Evaluate for malaria.
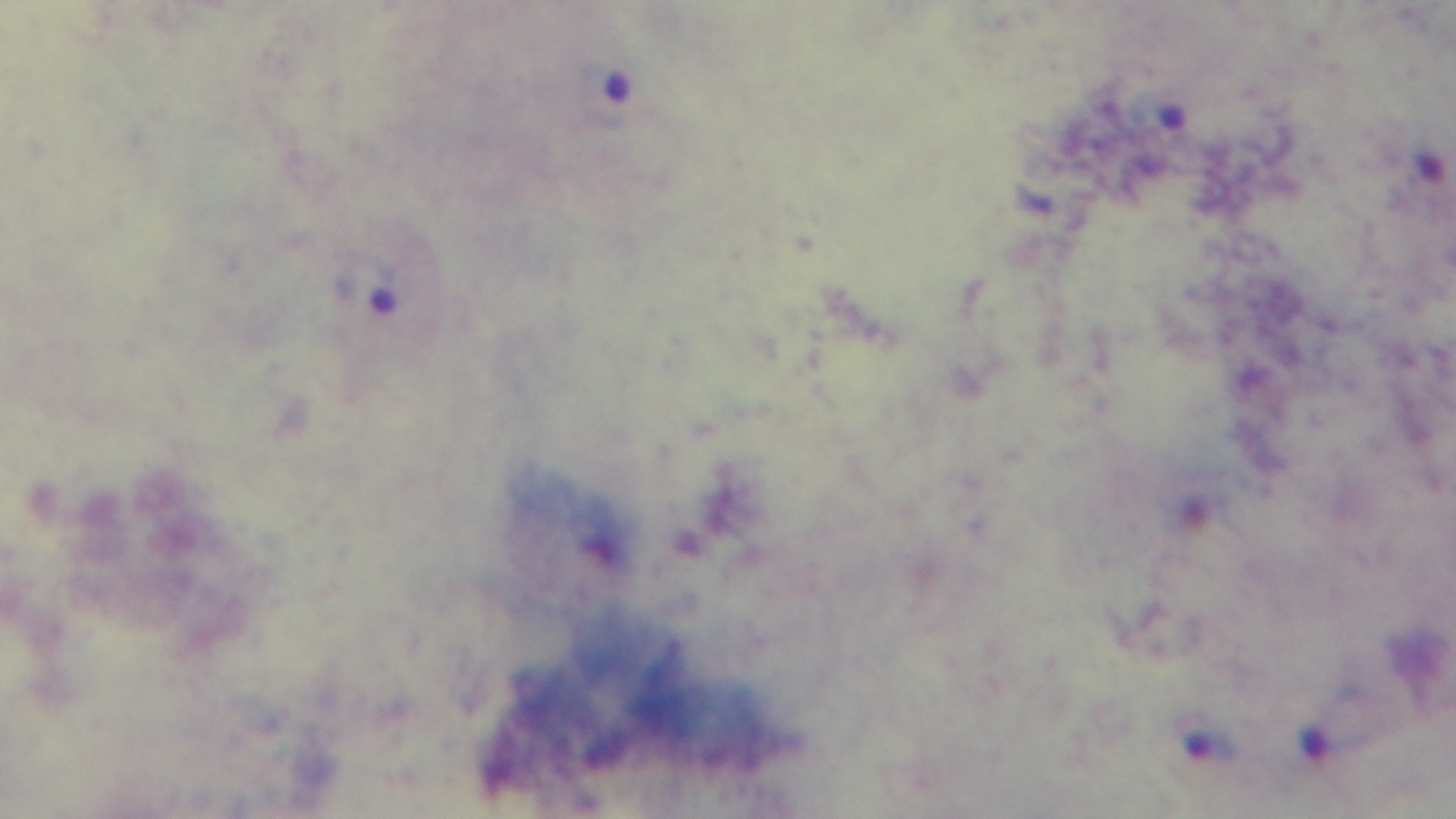
It is infected.

modality = light microscopy
capture = mounted 4K digital camera
field of view = one from the slide
stain = Giemsa
objective = 100x oil immersion
preparation = thick smear